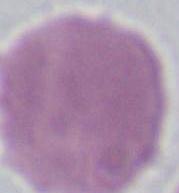

identification = red blood cell
modality = photomicrograph
magnification = 1000x